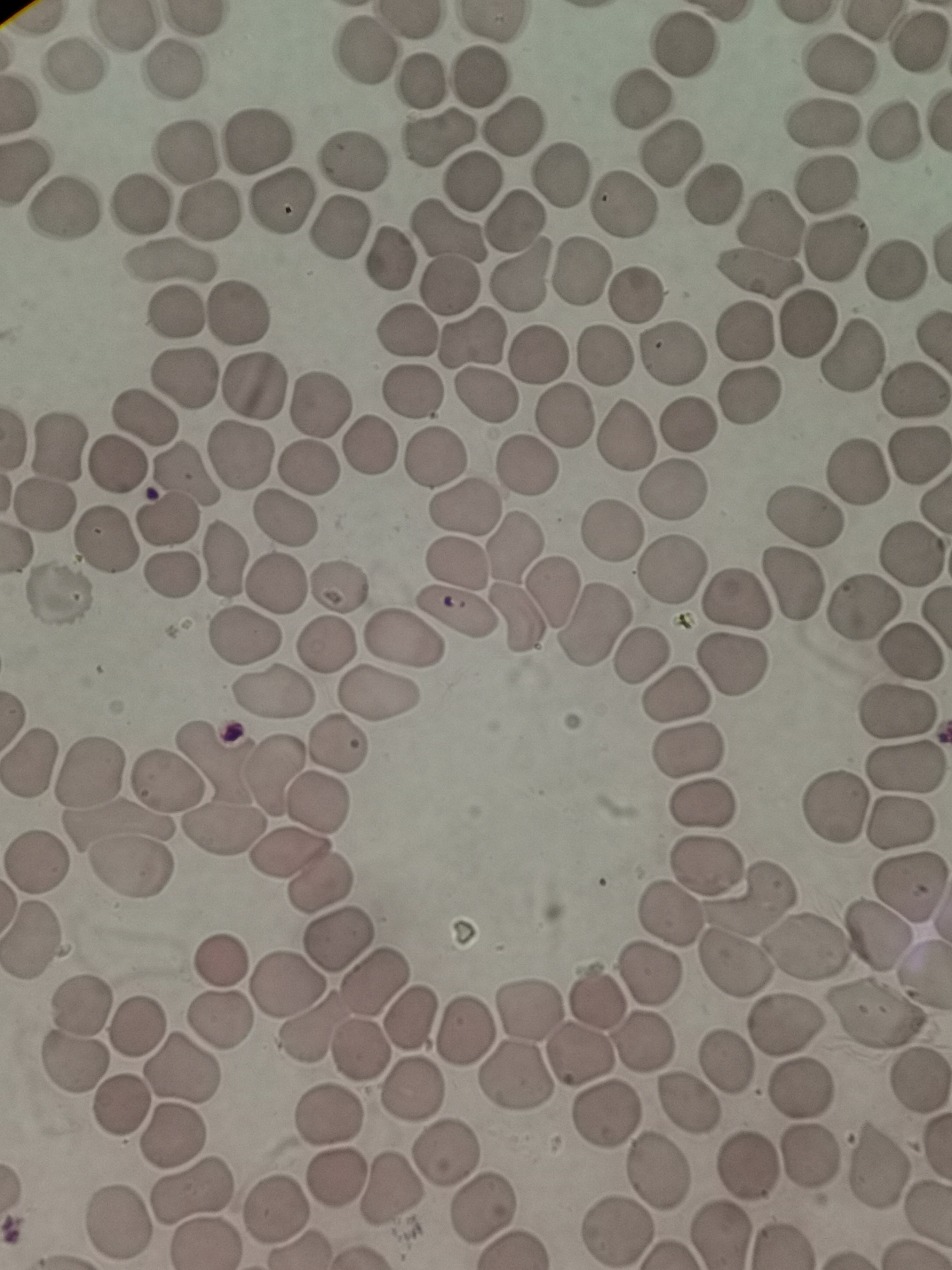

cell locations = approximate centers as (x, y) in pixels: (914, 40), (684, 44), (362, 49), (838, 65), (73, 66), (174, 70), (477, 76), (420, 79), (641, 99), (822, 123), (515, 124), (895, 128), (437, 136), (258, 140), (186, 151), (671, 153), (354, 158), (559, 170), (469, 180), (828, 182), (711, 190), (281, 201), (139, 204), (623, 206), (66, 211), (210, 211), (510, 219), (770, 222), (341, 225), (448, 228), (837, 250), (388, 258), (170, 259), (895, 269), (581, 270), (516, 273), (757, 273), (450, 286), (635, 295), (172, 311), (238, 312), (808, 323), (742, 330), (406, 331), (473, 338), (539, 352), (673, 354), (604, 356), (852, 358), (182, 377), (254, 386), (912, 392), (411, 393), (749, 393), (485, 396), (319, 404), (143, 415), (565, 417), (687, 424), (624, 434), (56, 440), (368, 445), (918, 456), (243, 458), (435, 459), (527, 464), (119, 466), (308, 469), (858, 472), (187, 473), (673, 488), (466, 506), (43, 508), (284, 516), (803, 516), (166, 518), (610, 530), (106, 541), (517, 545), (910, 556), (225, 558), (456, 564), (671, 567), (172, 575), (276, 582), (793, 583), (337, 586), (60, 594), (552, 594), (736, 599), (862, 610), (455, 613), (513, 617), (595, 626), (247, 635), (405, 640), (328, 643), (911, 651), (639, 657), (732, 666), (270, 692), (677, 695), (375, 696), (901, 715), (337, 742), (688, 751), (215, 759), (28, 761), (902, 769), (90, 771), (272, 774), (167, 778), (317, 802), (704, 805), (832, 806), (902, 825), (223, 831), (289, 855), (37, 860), (128, 864), (706, 864), (321, 884), (909, 884), (750, 893), (668, 914), (880, 936), (34, 942), (339, 942), (805, 945), (218, 961), (734, 963), (649, 972), (374, 977), (289, 983), (80, 1001), (598, 1001), (530, 1009), (873, 1013), (221, 1018), (410, 1018), (136, 1024), (787, 1024), (308, 1026), (463, 1030), (644, 1040), (361, 1050), (579, 1053), (726, 1064), (72, 1065), (184, 1069), (516, 1075), (798, 1086), (411, 1091), (687, 1101), (119, 1108), (604, 1115), (330, 1116), (170, 1138), (447, 1150), (810, 1157), (879, 1162), (748, 1164), (660, 1173), (338, 1175), (391, 1189), (193, 1193), (277, 1208), (485, 1208), (119, 1221), (616, 1229), (719, 1234), (206, 1243)
stain = Giemsa
capture = smartphone camera at the microscope eyepiece
preparation = thin smear
field of view = single
image size = 952×1270 pixels